Identify the parasite.
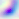

This is Toxoplasma gondii.

400x magnification. Photomicrograph.